Locate every Trypanosoma brucei.
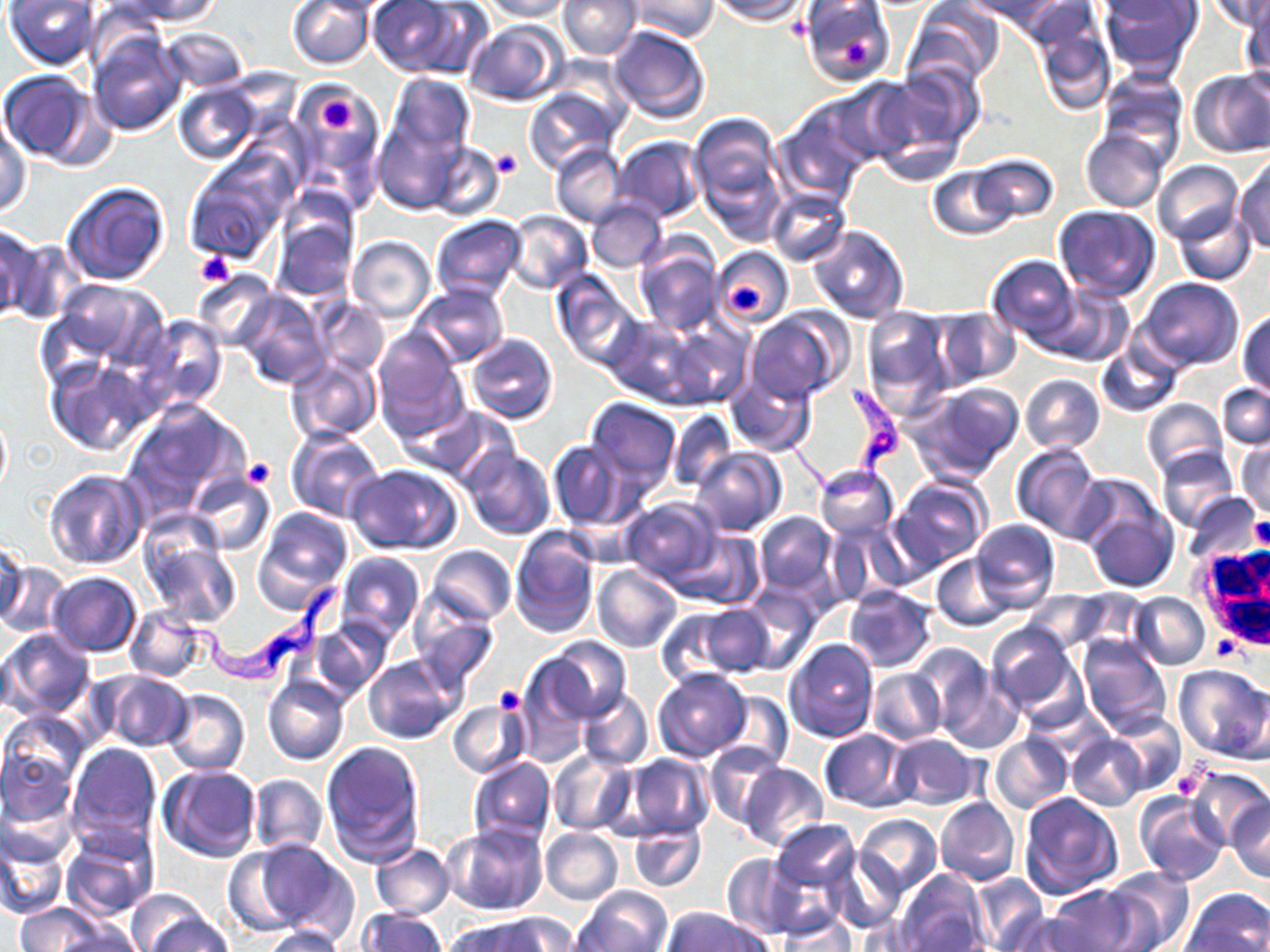

Approximate bounding boxes as named x1/y1/x2/y2 corners in pixels.
Trypanosoma brucei: (x1=775, y1=380, x2=905, y2=505), (x1=152, y1=578, x2=346, y2=692).

slide-level diagnosis = Trypanosoma brucei
preparation = thin blood film
modality = optical microscopy
stain = May-Grünwald-Giemsa
magnification = 1000x
uninfected red blood cell locations = approximate bounding boxes as named x1/y1/x2/y2 corners in pixels: (x1=4, y1=0, x2=102, y2=68), (x1=114, y1=0, x2=225, y2=26), (x1=288, y1=0, x2=374, y2=69), (x1=367, y1=0, x2=472, y2=77), (x1=484, y1=0, x2=571, y2=21), (x1=559, y1=0, x2=640, y2=59), (x1=628, y1=0, x2=719, y2=40), (x1=710, y1=0, x2=807, y2=23), (x1=974, y1=0, x2=1073, y2=32), (x1=1099, y1=0, x2=1202, y2=76), (x1=1210, y1=0, x2=1270, y2=33), (x1=1241, y1=0, x2=1269, y2=84), (x1=799, y1=1, x2=894, y2=87), (x1=904, y1=2, x2=1004, y2=89), (x1=1026, y1=5, x2=1116, y2=115), (x1=464, y1=18, x2=568, y2=105), (x1=608, y1=25, x2=710, y2=124), (x1=158, y1=28, x2=249, y2=93), (x1=88, y1=33, x2=186, y2=136), (x1=874, y1=63, x2=983, y2=169), (x1=1, y1=69, x2=103, y2=166), (x1=1097, y1=69, x2=1188, y2=162), (x1=1187, y1=69, x2=1270, y2=158), (x1=387, y1=74, x2=474, y2=159), (x1=295, y1=81, x2=380, y2=169), (x1=175, y1=84, x2=262, y2=164), (x1=524, y1=87, x2=620, y2=174), (x1=776, y1=102, x2=874, y2=202), (x1=688, y1=112, x2=786, y2=223), (x1=0, y1=114, x2=31, y2=219), (x1=372, y1=117, x2=462, y2=212), (x1=1081, y1=128, x2=1167, y2=212), (x1=614, y1=137, x2=706, y2=223), (x1=423, y1=141, x2=504, y2=222), (x1=550, y1=143, x2=627, y2=227), (x1=970, y1=154, x2=1058, y2=226), (x1=187, y1=156, x2=290, y2=263), (x1=1233, y1=158, x2=1270, y2=251), (x1=1152, y1=160, x2=1243, y2=245), (x1=927, y1=165, x2=1015, y2=242), (x1=61, y1=181, x2=172, y2=287), (x1=767, y1=187, x2=852, y2=267), (x1=586, y1=197, x2=667, y2=272), (x1=1052, y1=204, x2=1160, y2=300), (x1=1174, y1=206, x2=1257, y2=284), (x1=270, y1=210, x2=358, y2=304), (x1=505, y1=210, x2=593, y2=294), (x1=431, y1=214, x2=527, y2=301), (x1=1, y1=224, x2=43, y2=324), (x1=809, y1=225, x2=909, y2=324), (x1=347, y1=237, x2=434, y2=322), (x1=632, y1=241, x2=720, y2=337), (x1=711, y1=247, x2=795, y2=331), (x1=986, y1=254, x2=1080, y2=344), (x1=192, y1=270, x2=278, y2=352), (x1=552, y1=272, x2=642, y2=371), (x1=47, y1=277, x2=167, y2=376), (x1=1136, y1=277, x2=1244, y2=371), (x1=412, y1=283, x2=509, y2=368), (x1=1038, y1=284, x2=1134, y2=367), (x1=235, y1=293, x2=331, y2=391), (x1=312, y1=299, x2=388, y2=376), (x1=861, y1=306, x2=955, y2=406), (x1=933, y1=308, x2=1022, y2=389), (x1=747, y1=311, x2=846, y2=405), (x1=1237, y1=311, x2=1270, y2=397), (x1=604, y1=315, x2=703, y2=405), (x1=138, y1=316, x2=227, y2=411), (x1=661, y1=320, x2=751, y2=409), (x1=373, y1=328, x2=465, y2=435), (x1=466, y1=333, x2=558, y2=424), (x1=1094, y1=339, x2=1183, y2=419), (x1=284, y1=356, x2=381, y2=444), (x1=48, y1=358, x2=155, y2=455), (x1=726, y1=372, x2=817, y2=456), (x1=1020, y1=374, x2=1105, y2=453), (x1=908, y1=382, x2=1024, y2=484), (x1=1218, y1=382, x2=1269, y2=449), (x1=584, y1=397, x2=682, y2=493), (x1=1140, y1=398, x2=1228, y2=481), (x1=122, y1=400, x2=250, y2=522), (x1=428, y1=408, x2=517, y2=490), (x1=666, y1=408, x2=737, y2=492), (x1=0, y1=409, x2=11, y2=503), (x1=286, y1=429, x2=385, y2=521), (x1=546, y1=439, x2=629, y2=529), (x1=1235, y1=439, x2=1269, y2=517), (x1=1011, y1=443, x2=1103, y2=542), (x1=1156, y1=446, x2=1240, y2=532), (x1=690, y1=447, x2=785, y2=537), (x1=462, y1=449, x2=555, y2=539), (x1=347, y1=464, x2=463, y2=555), (x1=814, y1=464, x2=899, y2=540), (x1=43, y1=469, x2=148, y2=571), (x1=190, y1=472, x2=277, y2=556), (x1=889, y1=476, x2=990, y2=577), (x1=1076, y1=483, x2=1180, y2=594), (x1=1184, y1=492, x2=1261, y2=567), (x1=620, y1=497, x2=722, y2=586), (x1=253, y1=508, x2=353, y2=610), (x1=754, y1=512, x2=836, y2=595), (x1=827, y1=517, x2=907, y2=604), (x1=970, y1=518, x2=1059, y2=613), (x1=509, y1=527, x2=600, y2=638), (x1=669, y1=529, x2=764, y2=610), (x1=141, y1=532, x2=242, y2=629), (x1=0, y1=538, x2=30, y2=626), (x1=426, y1=545, x2=517, y2=625), (x1=335, y1=552, x2=424, y2=640), (x1=932, y1=554, x2=1014, y2=630), (x1=0, y1=560, x2=71, y2=639), (x1=593, y1=563, x2=681, y2=652), (x1=47, y1=572, x2=141, y2=657), (x1=739, y1=586, x2=822, y2=675), (x1=844, y1=586, x2=937, y2=671), (x1=1020, y1=590, x2=1110, y2=654), (x1=1130, y1=594, x2=1209, y2=669), (x1=695, y1=602, x2=773, y2=677), (x1=410, y1=603, x2=500, y2=694), (x1=126, y1=606, x2=205, y2=682), (x1=656, y1=610, x2=744, y2=688), (x1=310, y1=615, x2=394, y2=698), (x1=985, y1=621, x2=1081, y2=719), (x1=0, y1=627, x2=95, y2=719), (x1=545, y1=636, x2=629, y2=721), (x1=1078, y1=636, x2=1172, y2=736), (x1=785, y1=638, x2=880, y2=742), (x1=909, y1=644, x2=996, y2=733), (x1=363, y1=655, x2=464, y2=744), (x1=515, y1=658, x2=592, y2=765), (x1=1175, y1=664, x2=1270, y2=763), (x1=936, y1=666, x2=1023, y2=756), (x1=654, y1=668, x2=751, y2=761), (x1=91, y1=669, x2=194, y2=752), (x1=867, y1=669, x2=945, y2=745), (x1=263, y1=676, x2=350, y2=765), (x1=162, y1=689, x2=250, y2=774), (x1=578, y1=689, x2=654, y2=769), (x1=716, y1=691, x2=795, y2=771), (x1=449, y1=701, x2=530, y2=779), (x1=2, y1=711, x2=88, y2=791), (x1=1106, y1=712, x2=1187, y2=796), (x1=818, y1=728, x2=913, y2=811), (x1=990, y1=733, x2=1072, y2=815), (x1=887, y1=735, x2=981, y2=811), (x1=1068, y1=735, x2=1145, y2=810), (x1=320, y1=741, x2=425, y2=866), (x1=705, y1=741, x2=789, y2=828), (x1=67, y1=742, x2=163, y2=848), (x1=0, y1=748, x2=76, y2=828), (x1=548, y1=749, x2=636, y2=836), (x1=622, y1=754, x2=714, y2=839), (x1=467, y1=757, x2=556, y2=846), (x1=738, y1=762, x2=829, y2=852), (x1=159, y1=764, x2=262, y2=862), (x1=1186, y1=765, x2=1268, y2=845), (x1=248, y1=774, x2=327, y2=856), (x1=1017, y1=792, x2=1122, y2=900), (x1=1135, y1=792, x2=1228, y2=886), (x1=3, y1=793, x2=77, y2=867), (x1=935, y1=797, x2=1020, y2=885), (x1=1227, y1=797, x2=1270, y2=883), (x1=854, y1=815, x2=943, y2=894), (x1=768, y1=818, x2=860, y2=902), (x1=442, y1=821, x2=549, y2=917), (x1=628, y1=822, x2=707, y2=892), (x1=540, y1=828, x2=623, y2=904), (x1=62, y1=832, x2=156, y2=921), (x1=0, y1=835, x2=68, y2=919), (x1=249, y1=839, x2=357, y2=940), (x1=223, y1=844, x2=309, y2=936), (x1=371, y1=844, x2=453, y2=919), (x1=823, y1=847, x2=907, y2=935), (x1=720, y1=853, x2=803, y2=940), (x1=1100, y1=867, x2=1193, y2=952), (x1=894, y1=868, x2=992, y2=952), (x1=968, y1=872, x2=1049, y2=949), (x1=1048, y1=885, x2=1149, y2=952), (x1=576, y1=886, x2=673, y2=951), (x1=1181, y1=887, x2=1270, y2=952), (x1=127, y1=891, x2=217, y2=950), (x1=15, y1=903, x2=105, y2=952), (x1=661, y1=907, x2=772, y2=952), (x1=357, y1=908, x2=446, y2=952), (x1=777, y1=911, x2=858, y2=950), (x1=1007, y1=912, x2=1099, y2=952), (x1=144, y1=913, x2=233, y2=952), (x1=492, y1=913, x2=579, y2=951), (x1=450, y1=917, x2=554, y2=952), (x1=53, y1=924, x2=144, y2=952), (x1=261, y1=925, x2=349, y2=952)
field of view = one of a larger specimen
platelet locations = approximate bounding boxes as named x1/y1/x2/y2 corners in pixels: (x1=837, y1=33, x2=874, y2=70), (x1=320, y1=95, x2=357, y2=136), (x1=491, y1=148, x2=521, y2=178), (x1=195, y1=250, x2=234, y2=288), (x1=730, y1=284, x2=769, y2=316), (x1=243, y1=457, x2=274, y2=487), (x1=1251, y1=520, x2=1270, y2=549), (x1=1211, y1=638, x2=1242, y2=660), (x1=494, y1=685, x2=526, y2=717), (x1=1169, y1=764, x2=1204, y2=800)
white blood cell locations = approximate bounding boxes as named x1/y1/x2/y2 corners in pixels: (x1=1192, y1=544, x2=1270, y2=649)
image size = 1270×952 pixels